Comment on the morphology of the red blood cells.
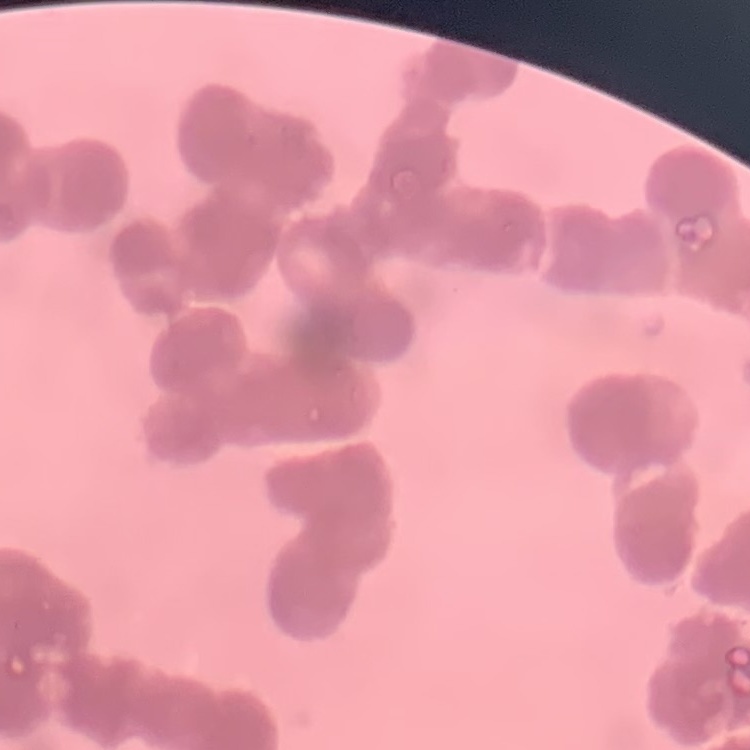

Rouleaux formation.

Thin blood smear. Square crop of a larger photomicrograph. Stained with either Field's or Giemsa.